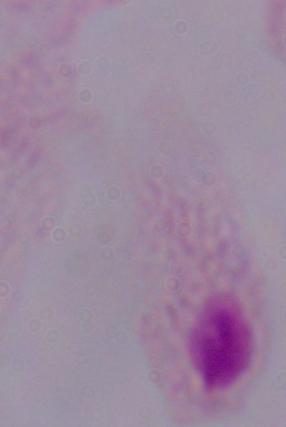

Summary:
  - Modality: photomicrograph
  - Magnification: 1000x
  - Identification: trichomonad